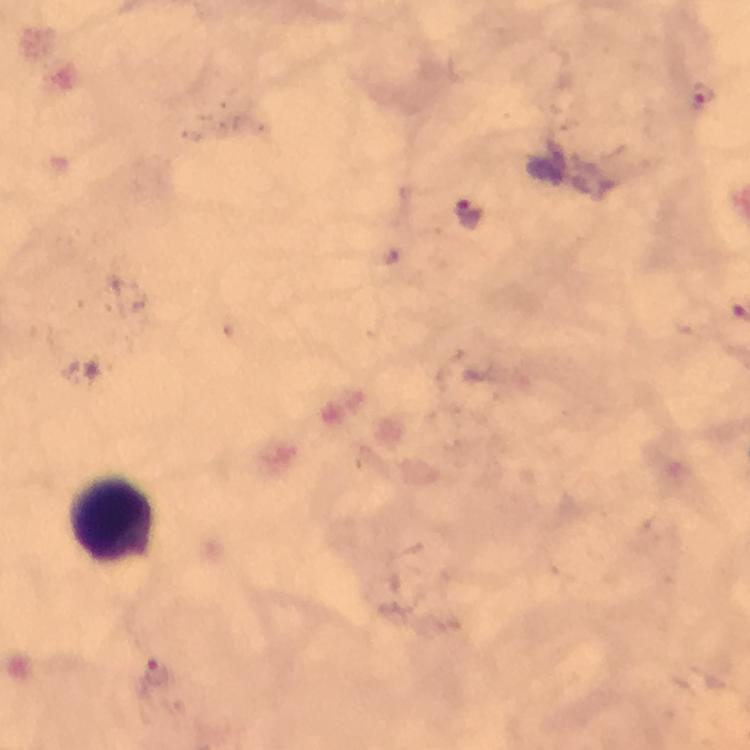

magnification = 100x
preparation = thick smear
malaria parasite locations = approximate centers as (x, y) in pixels: (702, 92), (470, 219), (156, 673)
stain = Giemsa
capture = smartphone photograph through a microscope
context = from a diagnostic examination for malaria
immersion oil = used
leukocyte locations = approximate centers as (x, y) in pixels: (114, 519)
cropped from = one field of view
image size = 750×750 pixels